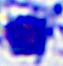
Summary:
  - Magnification: 400x
  - Identification: white blood cell
  - Modality: micrograph